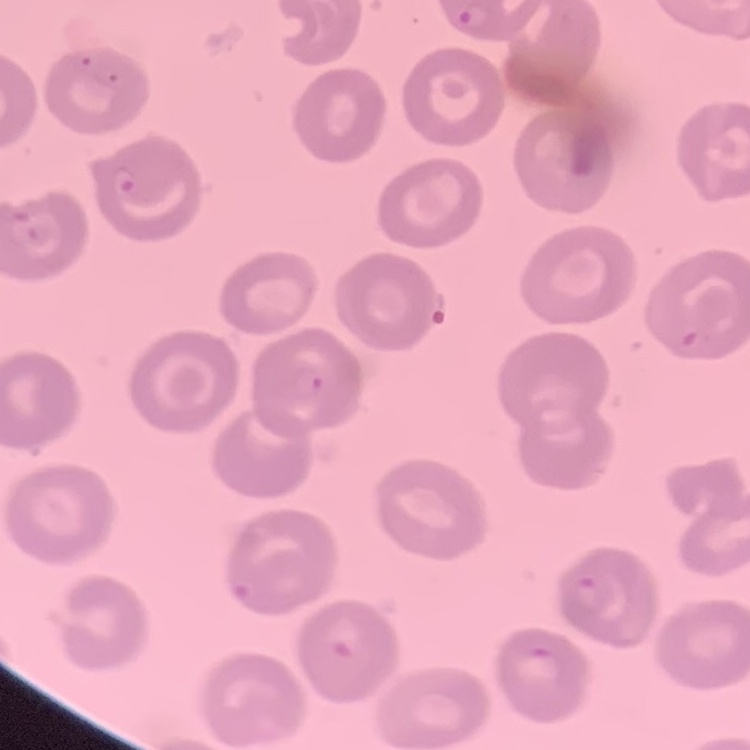

Summary:
  - Red blood cell morphology: no rouleaux formation
  - Stain: Field's or Giemsa
  - Preparation: thin blood film
  - Image type: one tile cut from a larger photomicrograph